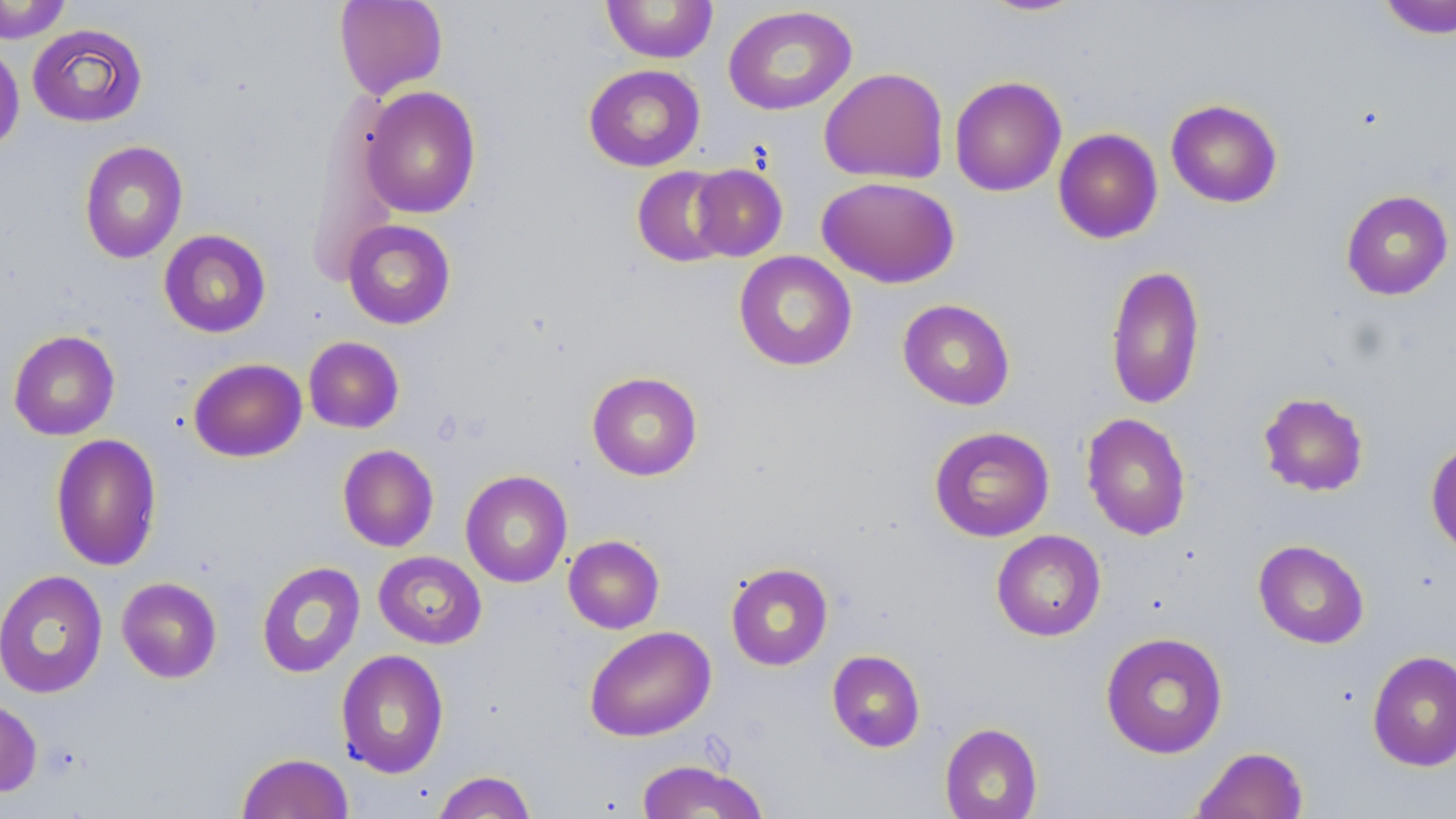

slide-level diagnosis = negative for blood parasites
uninfected red blood cell locations = approximate bounding boxes as named x1/y1/x2/y2 corners in pixels: (x1=334, y1=0, x2=448, y2=100), (x1=977, y1=0, x2=1088, y2=17), (x1=1376, y1=0, x2=1456, y2=39), (x1=0, y1=1, x2=72, y2=43), (x1=601, y1=1, x2=719, y2=64), (x1=722, y1=5, x2=857, y2=115), (x1=27, y1=24, x2=147, y2=127), (x1=0, y1=42, x2=24, y2=155), (x1=583, y1=64, x2=705, y2=172), (x1=819, y1=67, x2=949, y2=185), (x1=949, y1=76, x2=1067, y2=197), (x1=360, y1=86, x2=481, y2=219), (x1=1165, y1=98, x2=1283, y2=208), (x1=1053, y1=128, x2=1163, y2=244), (x1=78, y1=140, x2=188, y2=264), (x1=689, y1=163, x2=788, y2=261), (x1=631, y1=165, x2=736, y2=267), (x1=817, y1=176, x2=960, y2=288), (x1=1340, y1=189, x2=1454, y2=300), (x1=342, y1=220, x2=456, y2=329), (x1=159, y1=229, x2=271, y2=338), (x1=733, y1=251, x2=858, y2=371), (x1=1105, y1=264, x2=1205, y2=411), (x1=897, y1=298, x2=1016, y2=410), (x1=8, y1=329, x2=120, y2=441), (x1=303, y1=336, x2=405, y2=434), (x1=189, y1=358, x2=307, y2=462), (x1=586, y1=371, x2=703, y2=481), (x1=1258, y1=392, x2=1369, y2=496), (x1=1081, y1=413, x2=1192, y2=541), (x1=928, y1=426, x2=1055, y2=542), (x1=50, y1=433, x2=163, y2=572), (x1=1426, y1=438, x2=1456, y2=558), (x1=337, y1=444, x2=439, y2=552), (x1=460, y1=470, x2=573, y2=588), (x1=991, y1=529, x2=1106, y2=641), (x1=563, y1=535, x2=664, y2=633), (x1=1253, y1=539, x2=1369, y2=649), (x1=373, y1=551, x2=487, y2=649), (x1=256, y1=561, x2=366, y2=678), (x1=725, y1=562, x2=833, y2=671), (x1=0, y1=570, x2=108, y2=699), (x1=116, y1=577, x2=222, y2=683), (x1=584, y1=625, x2=716, y2=742), (x1=1100, y1=631, x2=1228, y2=759), (x1=335, y1=649, x2=449, y2=778), (x1=827, y1=649, x2=925, y2=753), (x1=1367, y1=649, x2=1456, y2=771), (x1=0, y1=696, x2=42, y2=797), (x1=939, y1=722, x2=1042, y2=819), (x1=1191, y1=745, x2=1308, y2=819), (x1=236, y1=752, x2=354, y2=818), (x1=635, y1=759, x2=770, y2=818), (x1=432, y1=770, x2=537, y2=819)
modality = light microscopy
preparation = thin blood film
image size = 1456×819 pixels
stain = May-Grünwald-Giemsa
field of view = one of a larger specimen
magnification = 1000x